Identify the preparation type.
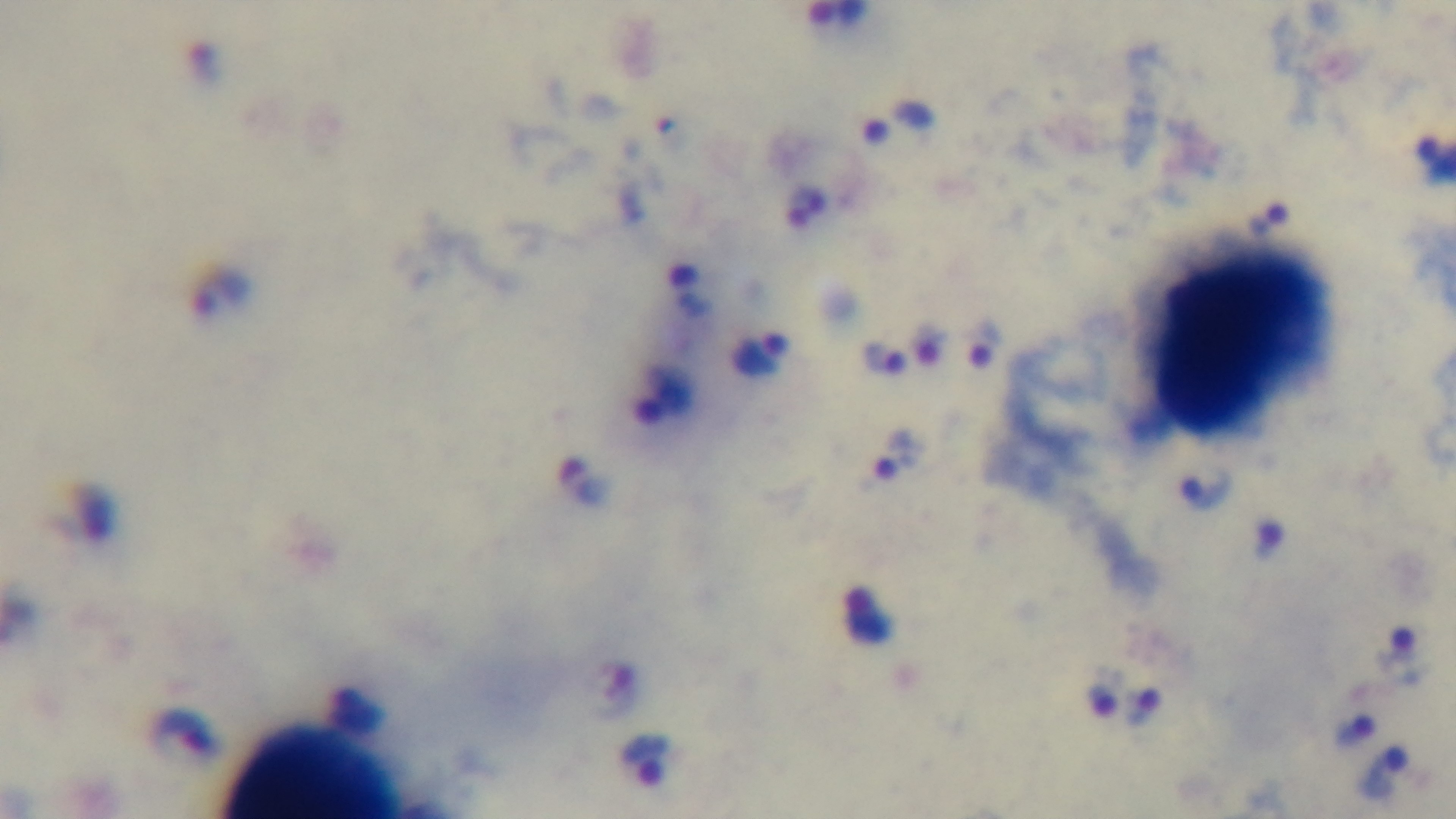
A thick smear.

Mounted 4K digital camera. Malaria status: infected. Giemsa-stained. One field from the slide. Photomicrograph. Oil-immersion objective, 100x.